Classify this cell by malaria status.
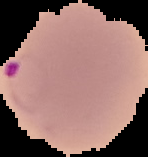
It is parasitized.

Summary:
  - Image type: segmented cell region with the area outside set to black
  - Image size: 148×157 pixels
  - Preparation: thin blood smear